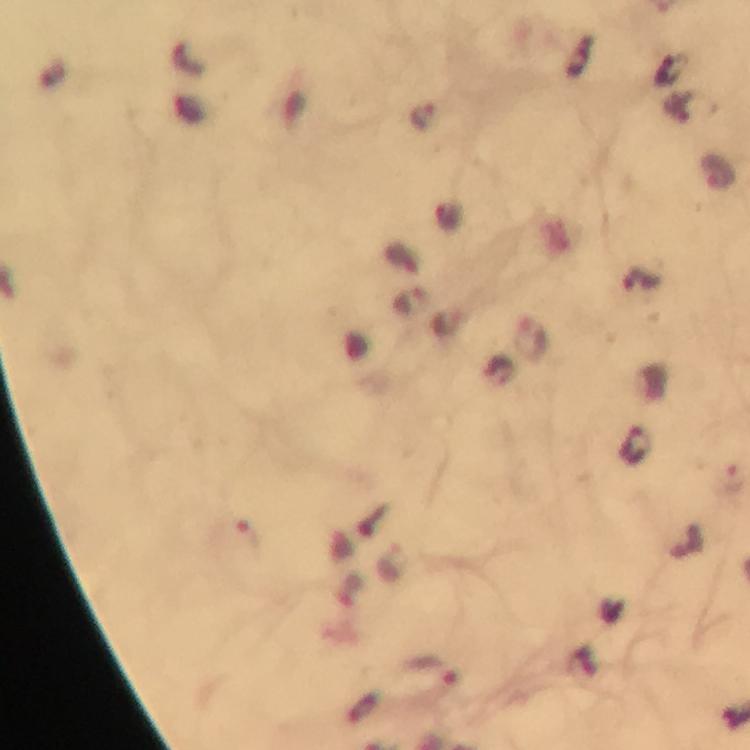

Approximate centers as [x, y] in pixels. Plasmodium parasite locations: [719, 172], [642, 278], [531, 339], [635, 445], [434, 670]. At 100x magnification. Thick blood smear. Immersion oil was used. From a malaria diagnostic workup. Image is 750×750 pixels. Giemsa-stained preparation. Smartphone photograph taken through a microscope. A crop from one field of view.